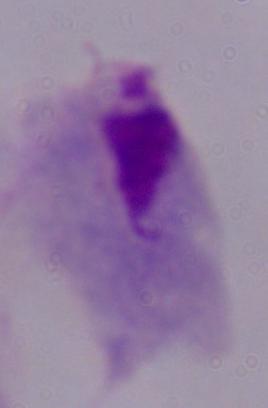
magnification: 1000x
modality: micrograph
identification: trichomonad